Classify this cell by malaria status.
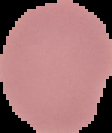

It is uninfected.

{
  "preparation": "thin blood film",
  "image_type": "segmented cell region with the area outside set to black",
  "image_size": "112×133 pixels"
}